Assess this cell for malaria.
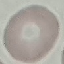
It is uninfected.

Summary:
  - Capture: smartphone camera at the microscope eyepiece
  - Image type: cell patch, automatically extracted from a larger field of view and resized to 64 × 64 pixels
  - Stain: Giemsa
  - Preparation: thin blood film